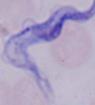
identification = trypanosome
modality = photomicrograph
magnification = 1000x